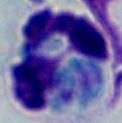
identification = white blood cell
modality = photomicrograph
magnification = 1000x